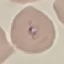

Malaria status: parasitized. Thin smear of blood. Photographed with a smartphone camera at the microscope eyepiece. Giemsa-stained preparation. Cell patch, automatically extracted from a larger field of view and resized to 64 × 64 pixels.